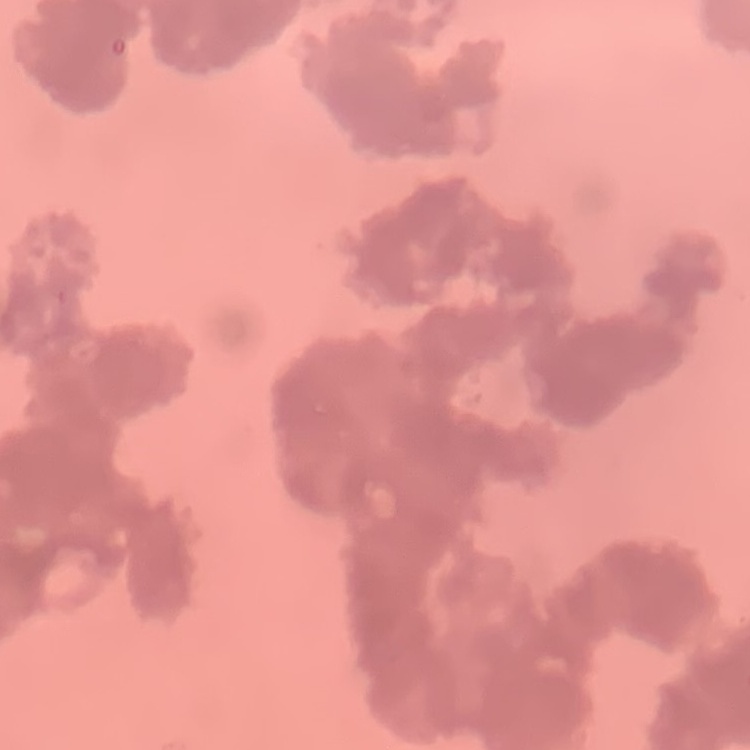

red blood cell morphology = rouleaux formation
stain = Field's or Giemsa
preparation = thin peripheral smear
image type = square crop of a larger photomicrograph